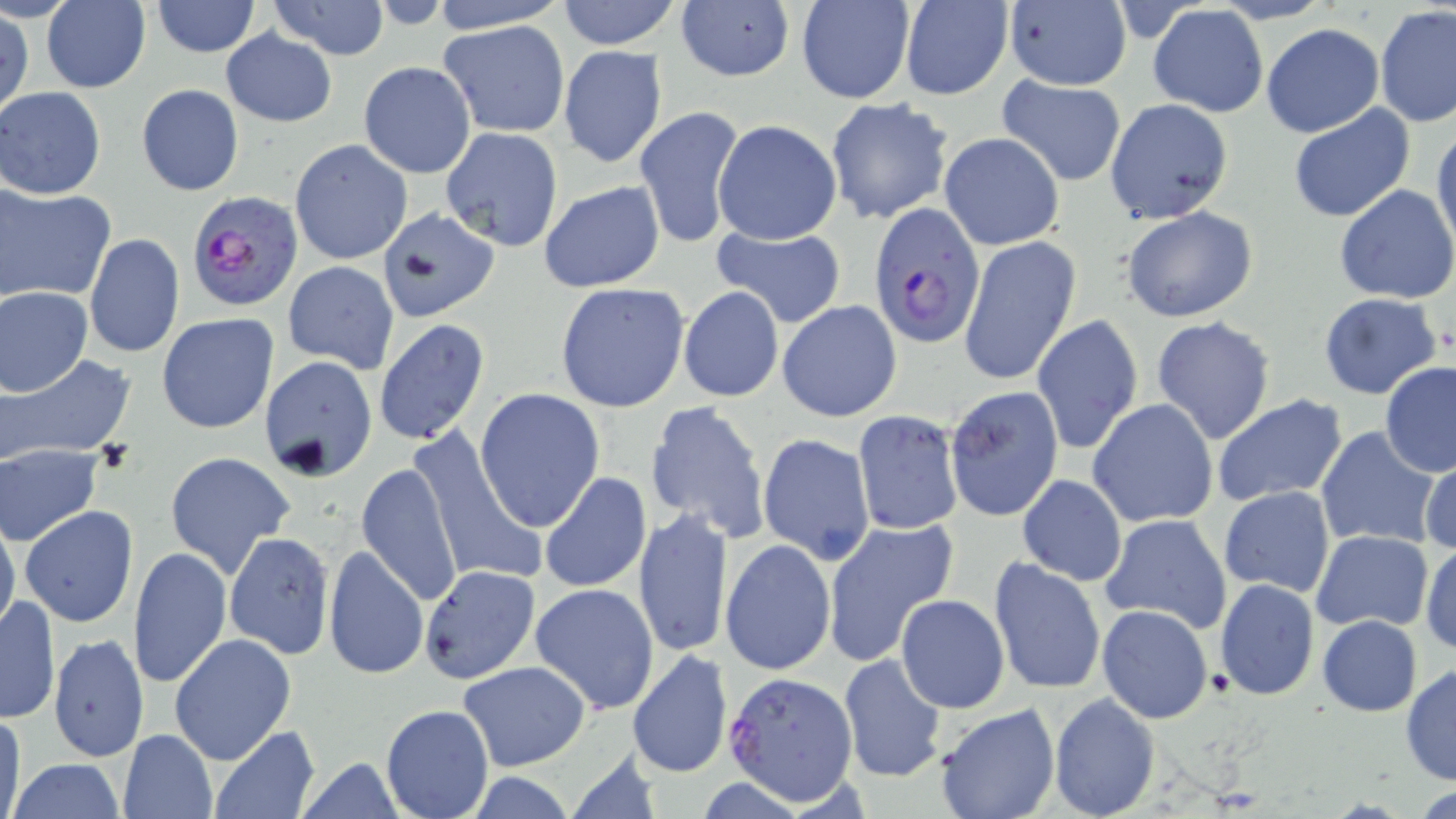
Approximate bounding boxes as (x1,y1)-(x2,y2) corner pairs in pixels. Plasmodium falciparum-infected red blood cell locations: (187,189)-(303,312), (868,203)-(986,346), (720,674)-(857,810). Uninfected red blood cell locations: (427,0)-(568,33), (556,0)-(683,49), (898,0)-(1014,100), (42,1)-(149,92), (150,1)-(260,57), (267,1)-(390,61), (795,1)-(916,104), (1001,1)-(1132,90), (674,2)-(795,84), (1148,5)-(1268,118), (1376,6)-(1456,128), (1,9)-(33,122), (436,21)-(571,137), (1260,23)-(1383,137), (221,29)-(337,127), (558,46)-(667,168), (358,61)-(475,177), (995,75)-(1127,187), (136,84)-(244,196), (1,87)-(105,199), (824,98)-(953,224), (1104,98)-(1234,226), (634,104)-(746,250), (1287,105)-(1417,223), (712,119)-(842,244), (1433,124)-(1456,256), (440,126)-(564,250), (939,132)-(1065,250), (289,139)-(413,266), (538,179)-(665,292), (1334,185)-(1456,303), (4,186)-(118,306), (1119,205)-(1260,323), (376,207)-(501,322), (709,227)-(847,329), (84,233)-(184,358), (958,234)-(1081,387), (283,260)-(399,373), (555,282)-(690,413), (677,286)-(784,402), (1,287)-(92,395), (1318,292)-(1444,401), (777,300)-(902,422), (157,313)-(278,433), (1029,315)-(1143,454), (1151,315)-(1277,445), (374,319)-(490,447), (259,355)-(378,482), (3,356)-(134,464), (1380,362)-(1456,478), (945,384)-(1064,522), (474,388)-(604,531), (1211,394)-(1347,507), (1088,399)-(1219,530), (644,400)-(770,544), (851,409)-(963,536), (1244,411)-(1404,534), (407,425)-(549,590), (1315,427)-(1441,550), (758,431)-(875,563), (1,446)-(103,545), (165,451)-(295,578), (1419,454)-(1455,557), (355,462)-(463,607), (540,471)-(652,595), (1016,473)-(1127,586), (1219,486)-(1335,598), (19,505)-(139,628), (634,507)-(732,660), (1100,513)-(1232,635), (0,514)-(20,640), (823,518)-(959,666), (1311,529)-(1433,634), (225,531)-(334,658), (721,540)-(835,676), (1420,541)-(1456,656), (322,545)-(428,681), (130,547)-(232,689), (989,556)-(1107,696), (422,564)-(540,685), (1214,578)-(1320,701), (531,583)-(659,713), (920,588)-(1089,711), (896,594)-(1009,713), (1,595)-(60,724), (1097,604)-(1213,724), (1317,614)-(1423,716), (169,633)-(295,764), (49,634)-(147,760), (626,649)-(733,780), (837,653)-(947,784), (458,660)-(590,772), (1401,664)-(1456,784), (1048,690)-(1159,818), (381,703)-(493,819), (935,704)-(1058,819), (0,708)-(26,819), (212,728)-(321,818), (118,730)-(215,817), (7,759)-(127,817), (293,759)-(410,818). Slide-level diagnosis: Plasmodium falciparum. Image is 1456×819 pixels. One field of a larger specimen. Thin blood smear. 1000x magnification. May-Grünwald-Giemsa-stained preparation. Optical microscopy.